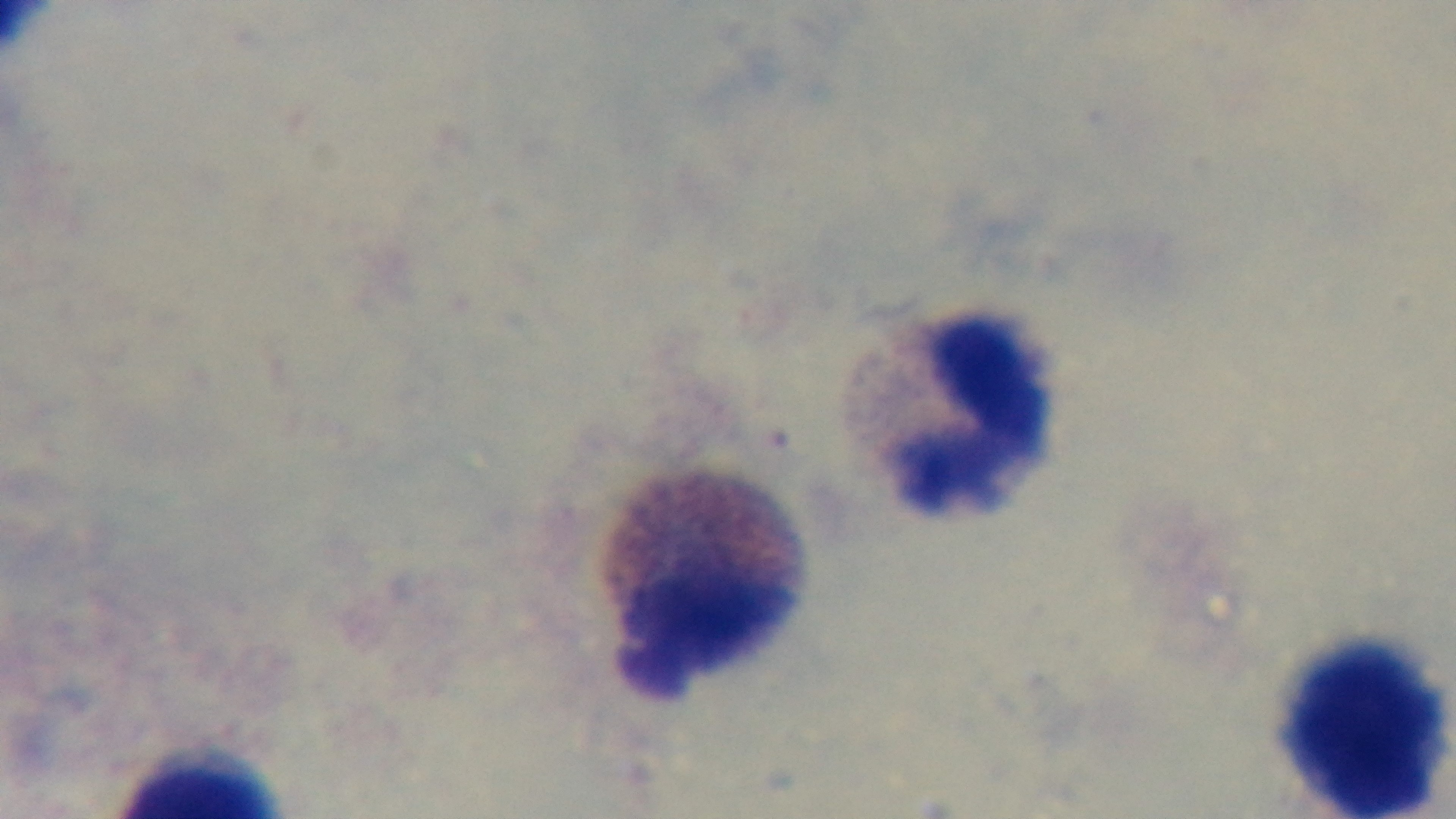

Summary:
  - Modality: light microscopy
  - Objective: 100x oil immersion
  - Field of view: one from the slide
  - Malaria status: uninfected
  - Capture: mounted 4K digital camera
  - Stain: Giemsa
  - Preparation: thick